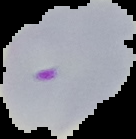
image_type: segmented cell region on a black background
preparation: thin blood film
image_size: 136×139 pixels
result: Plasmodium parasites detected